State which parasite is depicted.
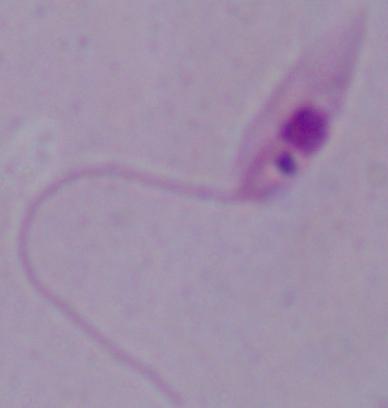

Leishmania.

modality = micrograph
magnification = 1000x